State which cell type is depicted.
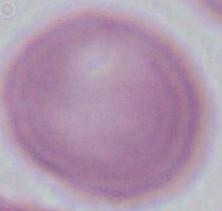

An erythrocyte.

magnification: 1000x
modality: photomicrograph